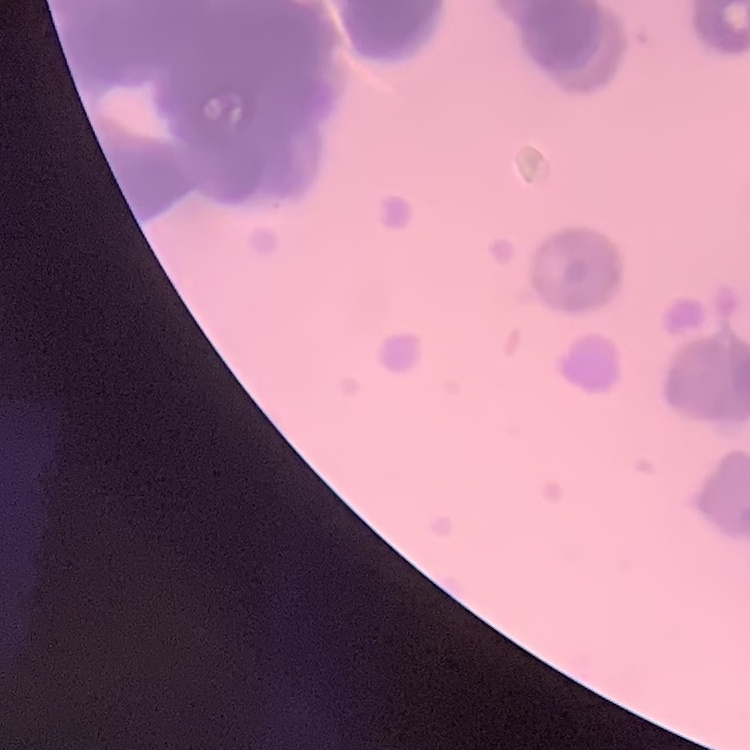

Summary:
  - Red blood cell morphology: rouleaux formation
  - Image type: square crop of a larger photomicrograph
  - Preparation: thin blood smear
  - Stain: Field's or Giemsa